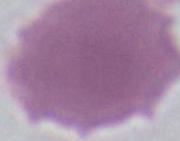
modality = micrograph
identification = red blood cell
magnification = 1000x